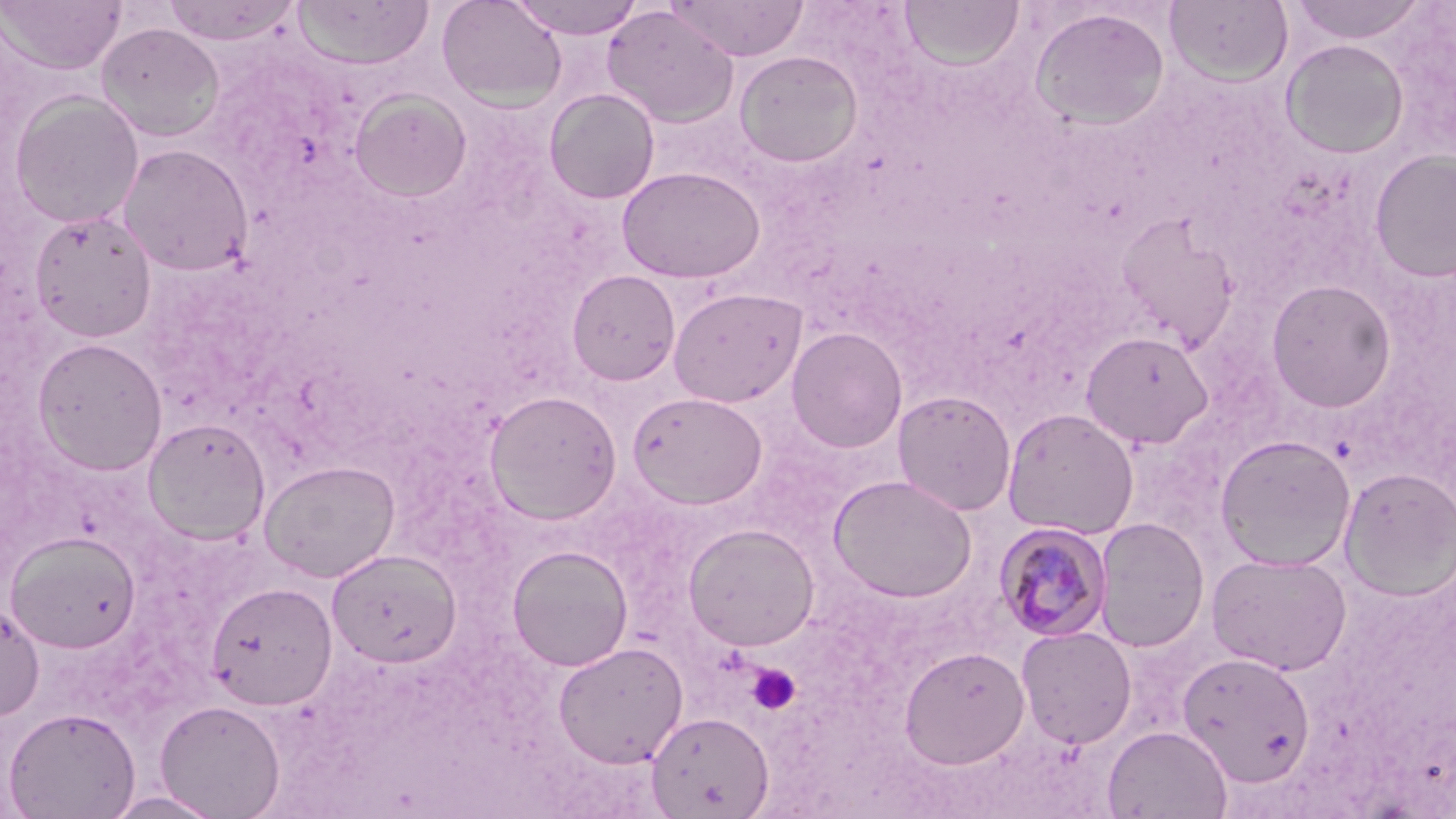

Approximate bounding boxes as [x1, y1, x2, y2] in pixels. Platelet locations: [747, 663, 801, 715]. Plasmodium malariae-infected red blood cell locations: [994, 522, 1113, 642]. Uninfected red blood cell locations: [436, 0, 568, 110], [508, 0, 647, 39], [667, 0, 810, 61], [899, 0, 1026, 71], [1289, 0, 1428, 44], [1, 1, 125, 74], [161, 1, 302, 46], [292, 1, 434, 70], [1164, 1, 1293, 85], [602, 6, 739, 127], [1029, 7, 1171, 131], [96, 22, 225, 141], [1281, 39, 1409, 159], [735, 50, 863, 169], [544, 88, 660, 204], [349, 89, 472, 202], [8, 91, 145, 228], [117, 143, 254, 276], [1369, 148, 1456, 283], [616, 166, 766, 283], [29, 209, 157, 342], [1115, 212, 1239, 351], [566, 269, 680, 385], [1265, 278, 1397, 412], [668, 287, 807, 407], [787, 327, 907, 453], [1079, 330, 1215, 450], [33, 337, 168, 474], [484, 389, 622, 525], [893, 389, 1016, 516], [628, 391, 768, 509], [1001, 407, 1140, 540], [142, 417, 271, 544], [1214, 434, 1357, 572], [259, 460, 401, 583], [1338, 467, 1456, 600], [828, 474, 978, 602], [1094, 517, 1211, 653], [683, 523, 820, 651], [6, 531, 140, 653], [507, 545, 633, 671], [328, 548, 463, 667], [1206, 551, 1352, 675], [206, 581, 338, 711], [0, 600, 45, 721], [1016, 626, 1137, 749], [553, 641, 689, 767], [899, 645, 1030, 768], [1177, 651, 1316, 786], [154, 699, 286, 818], [2, 706, 140, 819], [647, 711, 774, 818], [1102, 725, 1232, 819], [102, 790, 226, 819]. Slide-level diagnosis: Plasmodium malariae. Thin blood smear. Image is 1456×819 pixels. May-Grünwald-Giemsa-stained preparation. Single field of view. 1000x magnification. Light microscopy.